Point out each Plasmodium parasite.
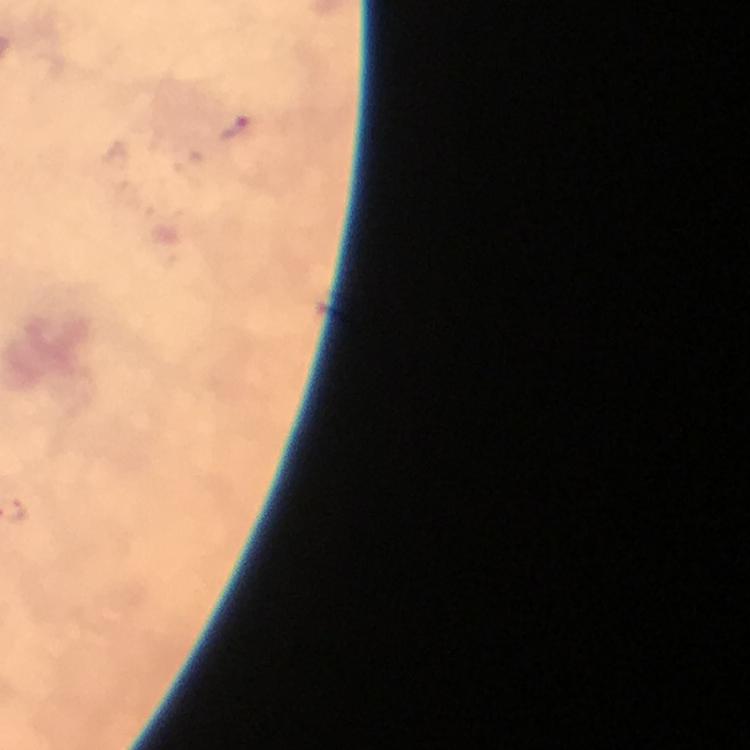

Approximate centers as {x, y} in pixels.
Plasmodium parasites: {235, 127}.

Summary:
  - Image size: 750×750 pixels
  - Preparation: thick blood smear
  - Context: from a diagnostic examination for malaria
  - Capture: smartphone camera through the microscope
  - Cropped from: one field of view
  - Stain: Giemsa
  - Magnification: 100x
  - Immersion oil: used